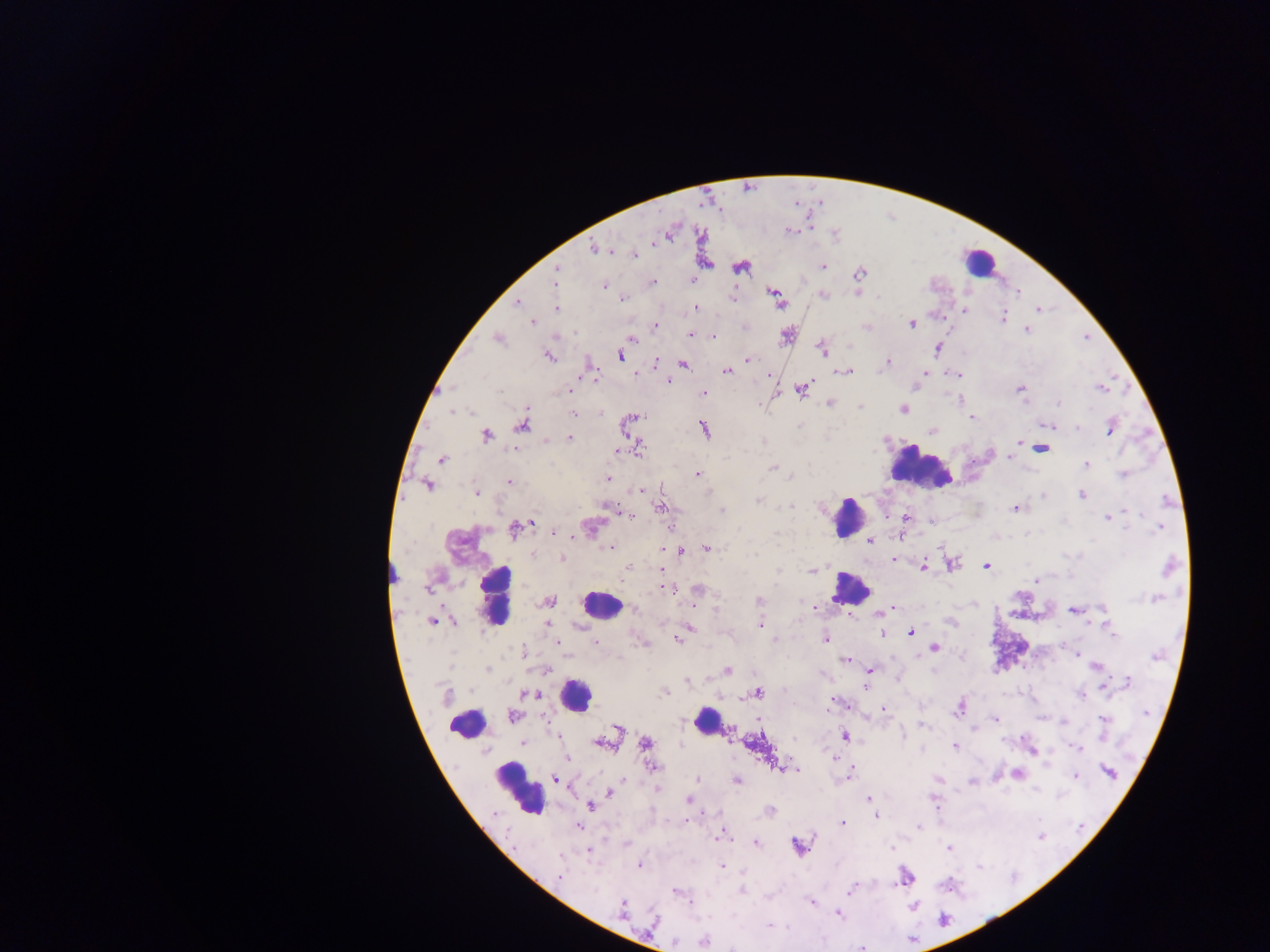

field of view = single
preparation = thick blood smear
leukocyte locations = approximate centers as [x, y] in pixels: [979, 263], [918, 466], [848, 518], [850, 589], [495, 594], [599, 605], [575, 694], [706, 720], [468, 722], [519, 789]
malaria parasite locations = approximate centers as [x, y] in pixels: [790, 231], [668, 233], [701, 234], [595, 249], [634, 254], [705, 264], [822, 265], [740, 267], [859, 273], [556, 277], [692, 281], [652, 282], [604, 286], [774, 292], [1018, 292], [823, 296], [623, 298], [777, 299], [519, 303], [695, 307], [556, 308], [1038, 309], [965, 310], [1002, 318], [533, 321], [911, 323], [654, 326], [1026, 329], [690, 334], [786, 336], [713, 337], [497, 338], [632, 338], [822, 348], [937, 348], [549, 356], [619, 356], [748, 361], [682, 362], [887, 363], [655, 364], [727, 371], [847, 371], [926, 373], [767, 375], [958, 375], [917, 377], [595, 378], [668, 380], [915, 386], [1102, 387], [801, 389], [1019, 389], [570, 390], [702, 393], [961, 398], [829, 403], [861, 408], [902, 409], [601, 412], [573, 414], [972, 417], [629, 421], [522, 423], [1047, 425], [1110, 426], [703, 429], [932, 431], [486, 434], [569, 438], [1019, 441], [1041, 447], [636, 448], [615, 451], [1011, 456], [442, 459], [1086, 464], [773, 467], [695, 473], [1123, 474], [607, 478], [509, 482], [427, 484], [641, 490], [476, 492], [1043, 494], [1081, 494], [758, 500], [661, 507], [1015, 507], [613, 508], [721, 511], [623, 513], [630, 513], [905, 516], [1107, 517], [931, 519], [531, 522], [526, 525], [590, 526], [516, 527], [1160, 528], [553, 533], [869, 541], [611, 547], [681, 548], [706, 548], [673, 549], [664, 550], [534, 555], [562, 558], [892, 559], [950, 564], [985, 565], [923, 566], [1169, 566], [627, 568], [812, 571], [1036, 580], [665, 587], [697, 590], [1155, 598], [759, 601], [547, 602], [693, 606], [814, 606], [891, 607], [633, 609], [1075, 610], [879, 613], [848, 614], [453, 620], [434, 622], [547, 623], [1106, 623], [760, 624], [687, 628], [910, 631], [882, 633], [683, 634], [678, 639], [773, 639], [827, 639], [595, 642], [934, 646], [523, 652], [1076, 653], [845, 660], [1097, 666], [486, 669], [545, 669], [727, 670], [869, 670], [686, 680], [1126, 683], [1104, 684], [865, 686], [664, 692], [757, 692], [531, 694], [1081, 694], [446, 695], [833, 701], [960, 707], [884, 710], [512, 716], [1102, 718], [995, 719], [758, 720], [921, 725], [615, 731], [729, 733], [845, 735], [558, 736], [523, 742], [602, 742], [645, 743], [955, 745], [1079, 748], [1031, 749], [567, 757], [836, 757], [651, 766], [779, 766], [796, 769], [1108, 772], [1017, 774], [1075, 775], [849, 776], [555, 778], [696, 779], [737, 780], [972, 782], [609, 792], [868, 799], [688, 800], [934, 801], [590, 805], [770, 811], [876, 815], [686, 819], [842, 822], [577, 826], [918, 828], [723, 835], [755, 843], [798, 846], [949, 848], [588, 850], [639, 864], [721, 867], [559, 877], [905, 877], [850, 889], [675, 891], [742, 891], [811, 900], [622, 909], [837, 913], [652, 921], [769, 925], [703, 940]
image size = 1270×952 pixels
country = Ghana
capture = mobile-phone photograph through a microscope